Classify this cell by malaria status.
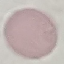
Uninfected.

Acquired by smartphone through the microscope eyepiece. Automatically extracted cell patch, resized to 64 × 64 pixels. Thin blood film. Giemsa stain.